Identify the parasite.
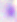
This is Toxoplasma gondii.

modality = micrograph
magnification = 400x